Locate and identify every blood parasite.
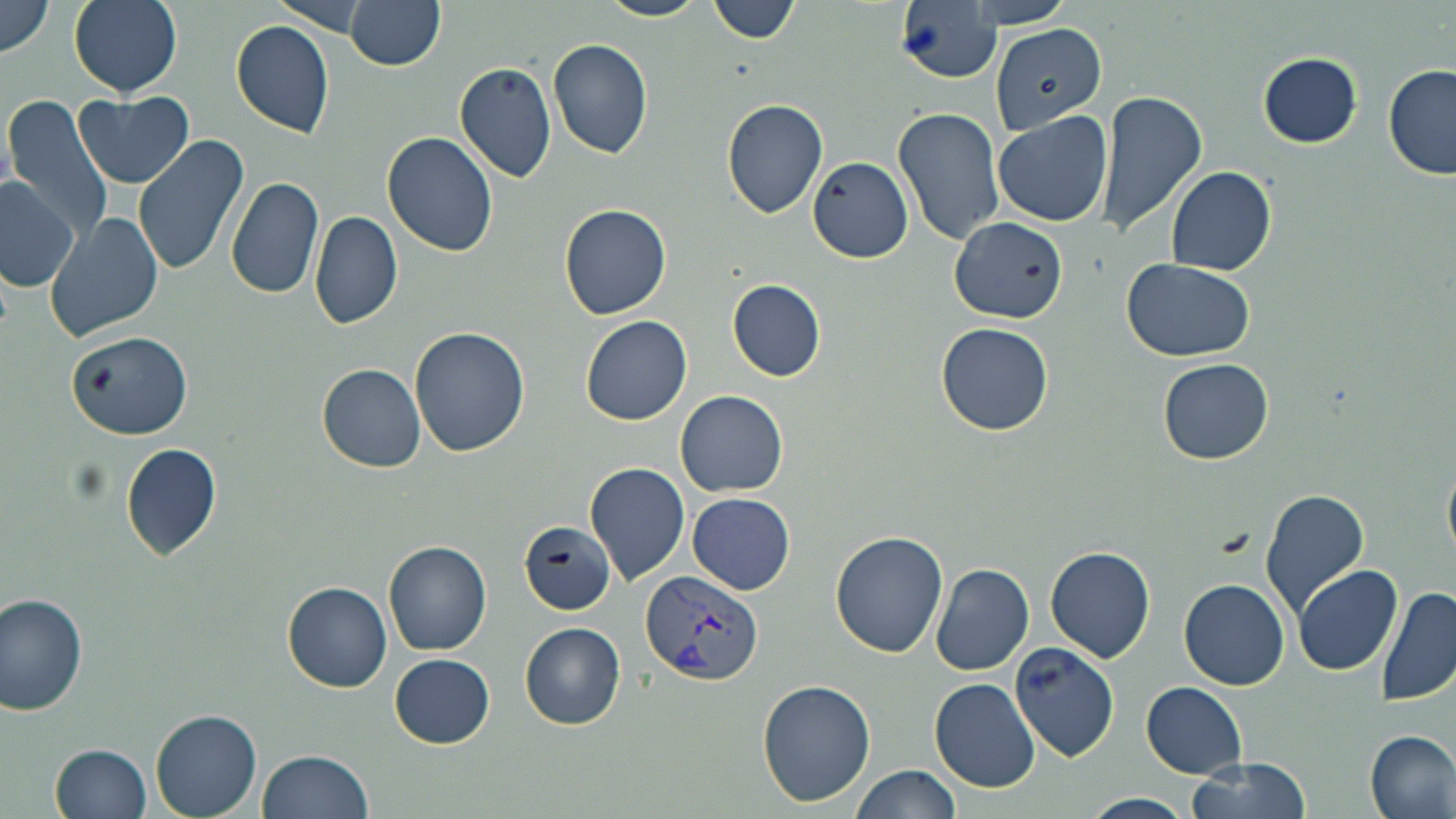

Approximate bounding boxes as [x1, y1, x2, y2] in pixels.
Plasmodium vivax-infected red blood cells: [640, 570, 763, 685].
No Plasmodium falciparum, Plasmodium ovale, Plasmodium malariae, Babesia divergens, or Trypanosoma brucei observed.

slide-level diagnosis = Plasmodium vivax
image size = 1456×819 pixels
field of view = single
preparation = thin blood smear
modality = optical microscopy
uninfected red blood cell locations = approximate bounding boxes as [x1, y1, x2, y2] in pixels: [69, 0, 182, 95], [270, 0, 378, 37], [595, 0, 708, 21], [899, 0, 1007, 84], [0, 1, 55, 61], [343, 1, 445, 70], [706, 1, 799, 45], [230, 19, 335, 138], [989, 22, 1109, 132], [548, 38, 653, 159], [1260, 53, 1363, 148], [454, 61, 556, 184], [1382, 64, 1456, 181], [1096, 91, 1208, 238], [75, 92, 194, 188], [3, 97, 114, 236], [722, 99, 829, 219], [894, 105, 1008, 248], [991, 110, 1115, 226], [134, 133, 250, 274], [381, 133, 499, 259], [808, 155, 913, 263], [1166, 166, 1277, 275], [227, 175, 326, 299], [0, 177, 80, 293], [560, 203, 672, 320], [44, 210, 164, 342], [310, 210, 403, 332], [950, 217, 1067, 322], [1123, 257, 1257, 361], [728, 279, 826, 380], [581, 316, 693, 426], [937, 323, 1052, 435], [411, 326, 530, 457], [67, 331, 193, 440], [1159, 359, 1274, 464], [318, 364, 427, 472], [676, 390, 789, 496], [120, 442, 221, 561], [1442, 450, 1456, 566], [585, 461, 690, 586], [1259, 490, 1370, 615], [687, 492, 796, 594], [519, 522, 614, 615], [831, 532, 947, 658], [384, 541, 493, 655], [1045, 545, 1154, 662], [929, 562, 1035, 677], [1295, 565, 1403, 676], [1180, 579, 1289, 689], [283, 582, 393, 692], [1377, 584, 1456, 706], [0, 591, 91, 716], [520, 623, 624, 728], [1008, 641, 1121, 763], [389, 654, 495, 748], [929, 678, 1041, 792], [758, 680, 876, 806], [1142, 682, 1247, 777], [151, 708, 263, 818], [1365, 730, 1455, 819], [52, 742, 151, 818], [257, 749, 373, 819], [1187, 758, 1312, 819], [848, 763, 961, 819], [1084, 792, 1193, 817]
magnification = 1000x
stain = May-Grünwald-Giemsa